Comment on the morphology of the red blood cells.
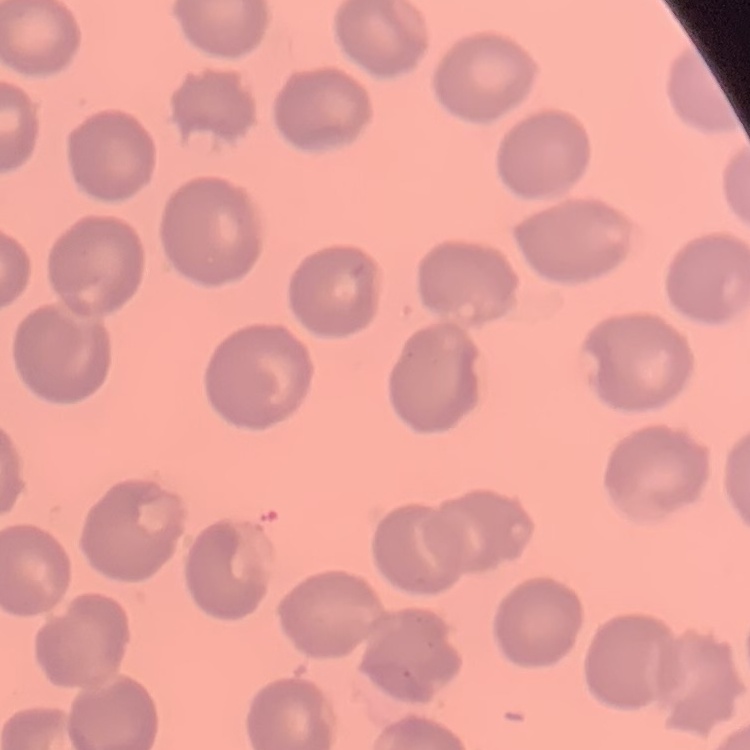

They show no rouleaux formation.

Thin peripheral smear. Field's or Giemsa stain. Square crop of a larger photomicrograph.